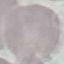

result = negative for malaria parasites
image type = cell patch, automatically extracted from a larger field of view and resized to 64 × 64 pixels
capture = smartphone camera at the microscope eyepiece
stain = Giemsa
preparation = thin smear